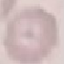
Summary:
  - Result: no malaria parasites seen
  - Preparation: thin blood film
  - Image type: automatically extracted cell patch, resized to 64 × 64 pixels
  - Capture: smartphone through the microscope eyepiece
  - Stain: Giemsa